Identify the parasite.
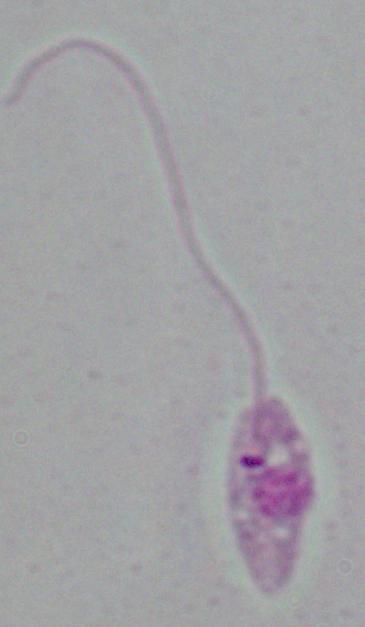
Leishmania.

{
  "magnification": "1000x",
  "modality": "photomicrograph"
}